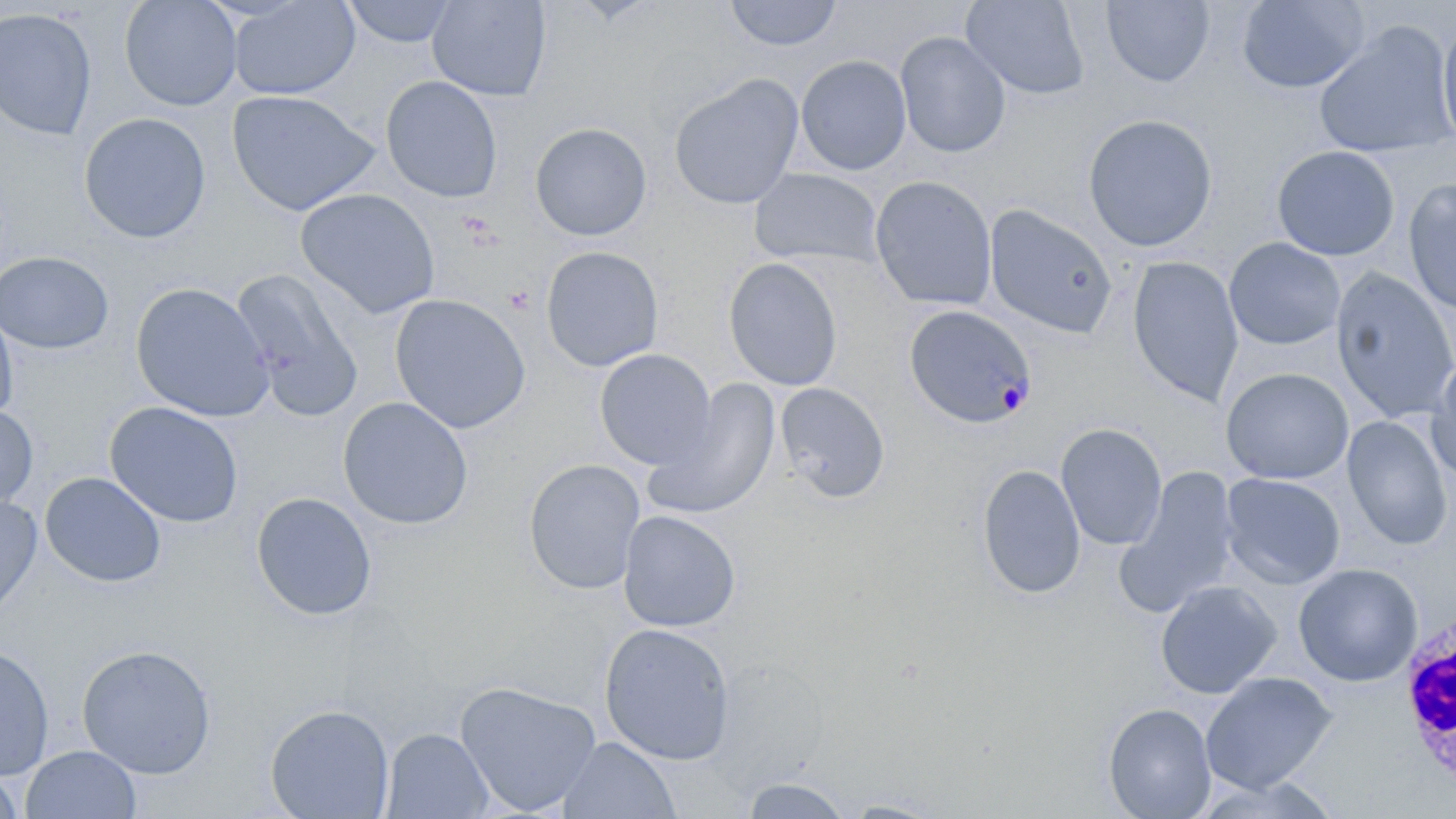 Approximate bounding boxes as (x1,y1)-(x2,y2) corner pairs in pixels. White blood cell locations: (1396,606)-(1455,788). Platelet locations: (504,285)-(534,315). Plasmodium malariae-infected red blood cell locations: (904,305)-(1036,427). Uninfected red blood cell locations: (119,0)-(242,112), (228,0)-(361,100), (341,0)-(459,48), (427,0)-(551,102), (724,0)-(842,51), (960,0)-(1090,100), (1236,0)-(1371,94), (1099,1)-(1215,86), (0,7)-(97,140), (1436,15)-(1456,154), (1313,22)-(1456,160), (894,31)-(1011,159), (795,54)-(912,176), (669,73)-(804,210), (380,75)-(503,203), (226,89)-(381,216), (78,112)-(212,244), (1082,113)-(1218,252), (530,122)-(652,241), (1272,145)-(1399,261), (749,168)-(884,268), (869,176)-(998,311), (1403,179)-(1456,316), (295,188)-(441,319), (984,204)-(1119,339), (1224,237)-(1346,350), (540,245)-(664,372), (0,251)-(114,355), (1126,256)-(1244,405), (722,257)-(843,391), (230,267)-(364,422), (1330,267)-(1456,424), (130,282)-(274,422), (389,293)-(531,434), (0,305)-(18,424), (594,349)-(718,471), (1426,355)-(1456,488), (1220,367)-(1355,484), (643,378)-(782,521), (774,382)-(890,503), (337,396)-(473,530), (106,402)-(244,528), (0,405)-(39,514), (1341,415)-(1454,550), (1055,423)-(1168,550), (523,458)-(646,595), (977,464)-(1086,600), (1117,466)-(1242,616), (40,472)-(167,588), (1219,473)-(1346,590), (251,492)-(377,621), (0,494)-(42,622), (618,510)-(741,632), (1293,563)-(1423,686), (1155,580)-(1281,699), (598,622)-(736,764), (0,644)-(55,780), (76,644)-(216,778), (1200,671)-(1337,793), (453,680)-(603,815), (1102,703)-(1217,818), (265,704)-(395,818), (381,728)-(494,818), (556,736)-(681,819), (20,745)-(142,819), (0,765)-(24,819), (1193,775)-(1344,819), (739,776)-(854,818), (840,800)-(946,818). Slide-level diagnosis: Plasmodium malariae. Image is 1456×819 pixels. Thin blood smear. May-Grünwald-Giemsa-stained preparation. Single field of view. Optical microscopy. Captured at 1000x magnification.